State which parasite is depicted.
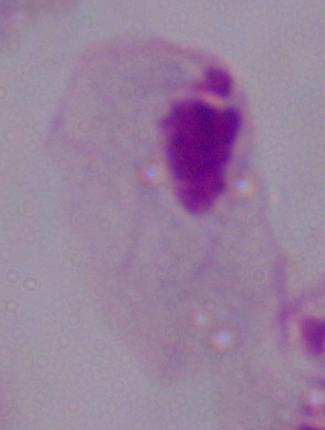
This is a trichomonad.

Micrograph. Captured at 1000x magnification.